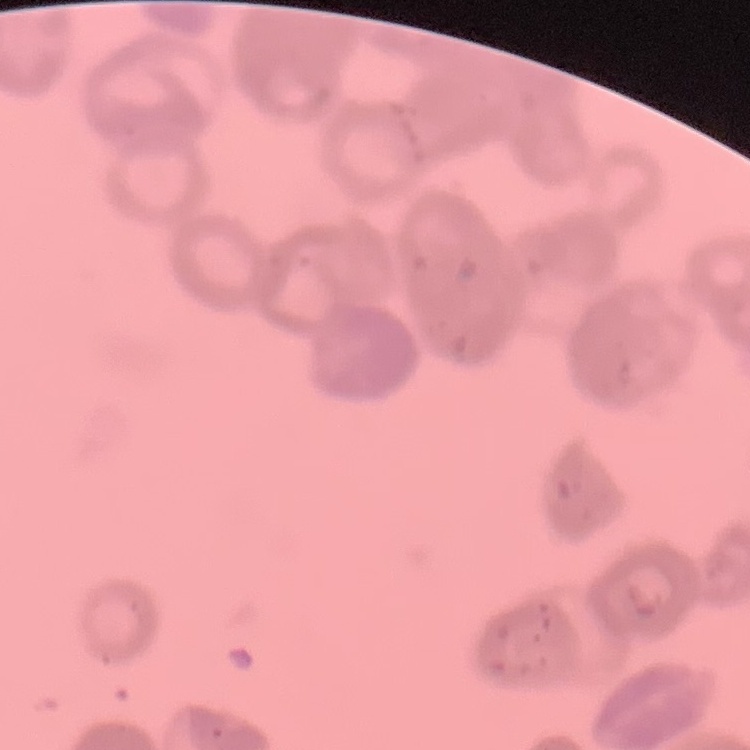

Summary:
  - Erythrocyte morphology: rouleaux formation
  - Image type: square crop of a larger photomicrograph
  - Preparation: thin blood smear
  - Stain: Field's or Giemsa